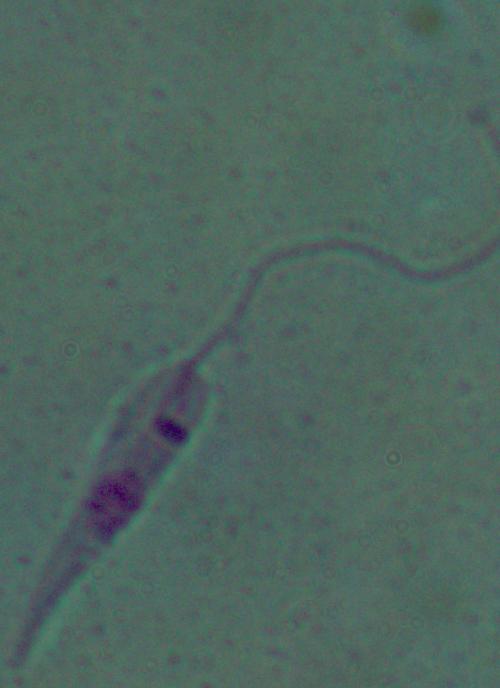
modality = photomicrograph
identification = Leishmania
magnification = 1000x